Locate and identify every blood parasite.
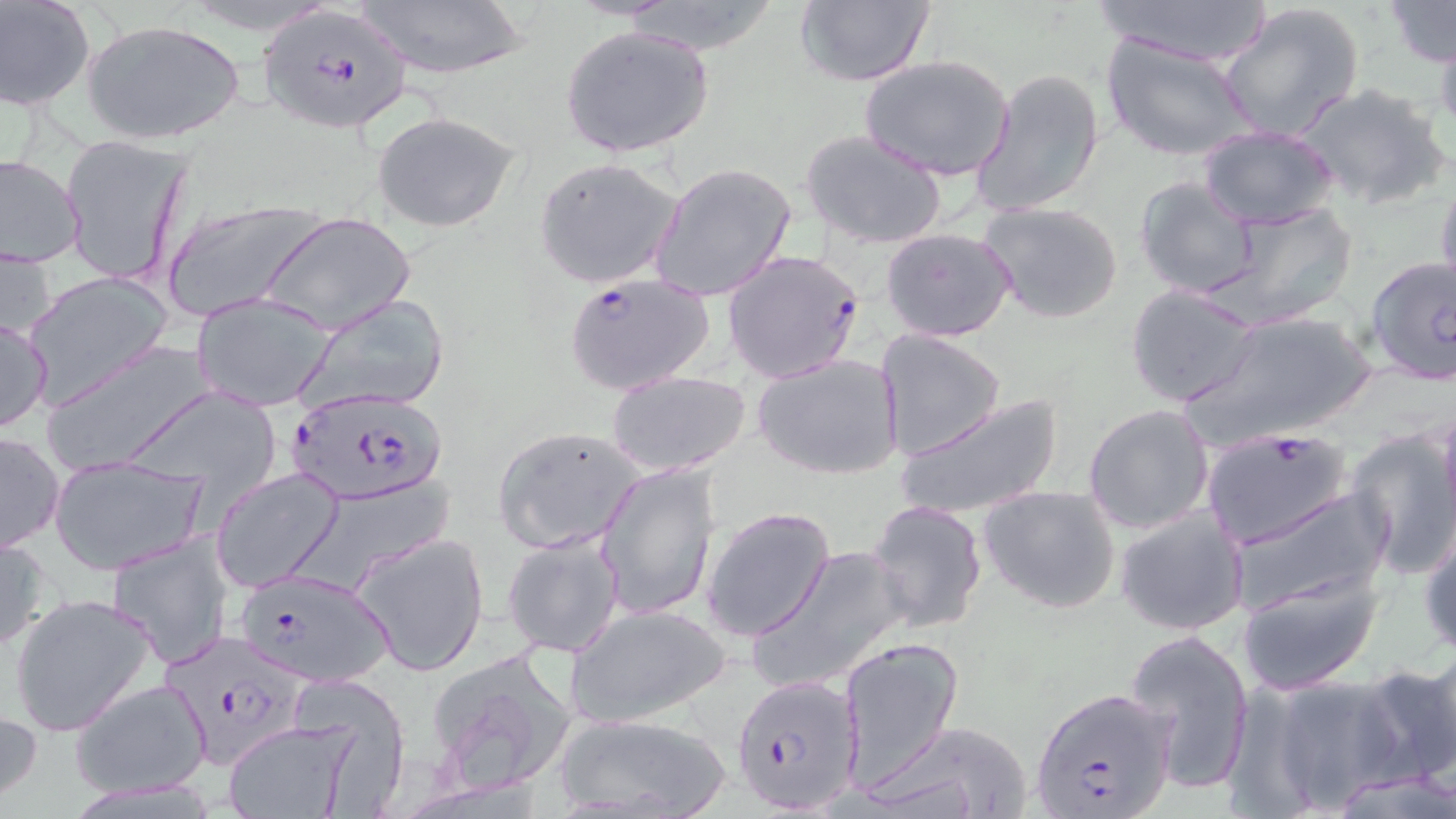
Approximate bounding boxes as [x1, y1, x2, y2] in pixels.
Plasmodium falciparum-infected red blood cells: [257, 12, 413, 123], [722, 248, 865, 383], [563, 271, 716, 397], [288, 386, 448, 505], [1201, 426, 1354, 550], [233, 567, 397, 690], [162, 629, 306, 775], [732, 677, 861, 814], [1033, 687, 1178, 819].
No Plasmodium ovale, Plasmodium malariae, Plasmodium vivax, Babesia divergens, or Trypanosoma brucei observed.

slide-level diagnosis = Plasmodium falciparum
modality = light microscopy
magnification = 1000x
preparation = thin blood film
image size = 1456×819 pixels
uninfected red blood cell locations = approximate bounding boxes as [x1, y1, x2, y2] in pixels: [351, 0, 530, 81], [792, 0, 936, 88], [1091, 0, 1274, 67], [1382, 0, 1455, 68], [0, 1, 94, 111], [1218, 2, 1365, 142], [81, 19, 247, 145], [558, 24, 715, 159], [1434, 27, 1456, 143], [1099, 33, 1257, 163], [860, 54, 1015, 183], [973, 68, 1105, 216], [1293, 82, 1451, 213], [373, 111, 521, 232], [1198, 125, 1339, 229], [800, 128, 949, 249], [62, 133, 191, 289], [1, 154, 84, 268], [533, 156, 683, 290], [647, 161, 796, 305], [1436, 169, 1456, 297], [1134, 177, 1260, 299], [163, 196, 324, 322], [977, 200, 1126, 325], [1213, 202, 1360, 328], [262, 211, 415, 334], [880, 226, 1016, 342], [0, 242, 55, 347], [1363, 256, 1455, 386], [25, 271, 173, 407], [1125, 283, 1264, 408], [192, 294, 336, 412], [298, 294, 451, 414], [1183, 310, 1379, 448], [0, 315, 51, 434], [874, 331, 1006, 462], [44, 342, 221, 476], [753, 352, 903, 481], [605, 370, 752, 476], [116, 384, 287, 500], [895, 393, 1066, 521], [1083, 404, 1216, 534], [492, 425, 647, 553], [1346, 428, 1456, 579], [1, 430, 65, 554], [49, 455, 208, 575], [595, 460, 721, 621], [212, 469, 345, 592], [978, 484, 1122, 616], [1230, 486, 1392, 615], [863, 500, 987, 635], [700, 505, 836, 642], [1115, 507, 1250, 637], [1418, 520, 1456, 662], [108, 531, 235, 669], [351, 531, 491, 677], [502, 532, 625, 659], [0, 535, 50, 652], [751, 546, 908, 692], [1237, 573, 1384, 695], [8, 593, 158, 737], [565, 602, 730, 730], [1124, 629, 1257, 791], [837, 637, 964, 789], [1421, 640, 1456, 776], [424, 646, 577, 799], [1354, 662, 1454, 791], [293, 675, 414, 810], [1267, 676, 1406, 811], [68, 679, 212, 800], [0, 701, 43, 807], [549, 711, 735, 819], [221, 719, 361, 819], [869, 721, 1036, 819], [1321, 770, 1456, 818]
stain = May-Grünwald-Giemsa
field of view = single